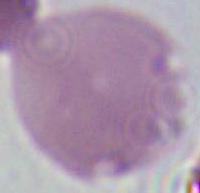

Summary:
  - Identification: erythrocyte
  - Modality: micrograph
  - Magnification: 1000x